Locate every leukocyte (white blood cell).
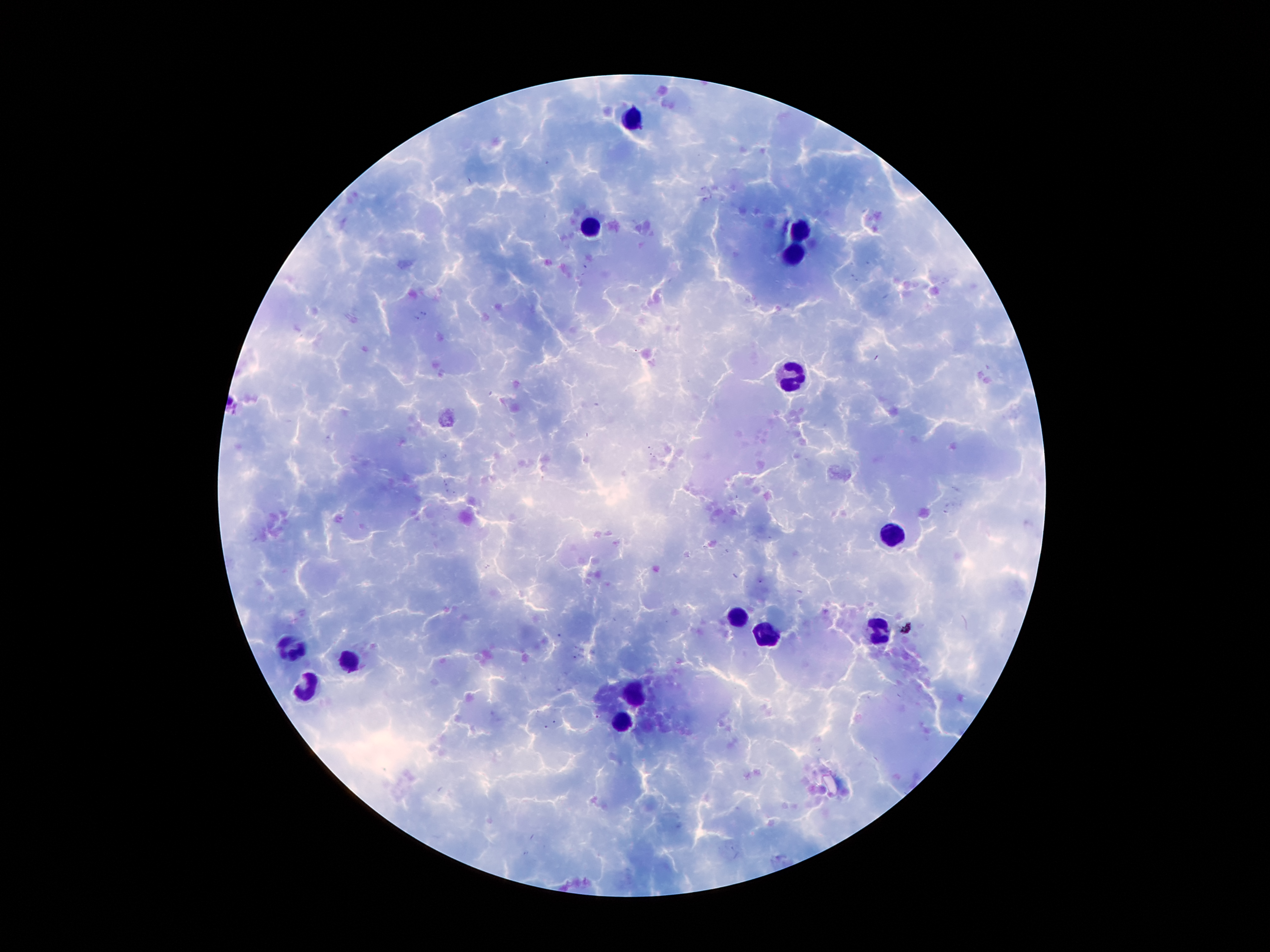
Approximate centers as {x, y} in pixels.
Leukocytes: {632, 121}, {592, 227}, {797, 228}, {794, 255}, {796, 374}, {893, 538}, {738, 617}, {880, 629}, {766, 638}, {287, 650}, {354, 658}, {308, 691}, {634, 695}, {625, 720}.

Summary:
  - Patient malaria status: infected with Plasmodium falciparum
  - Capture: smartphone camera through the microscope eyepiece
  - Malaria parasites: not seen
  - Stain: Giemsa
  - Field of view: one from this slide
  - Image size: 1270×952 pixels
  - Magnification: 100x
  - Preparation: thick blood smear